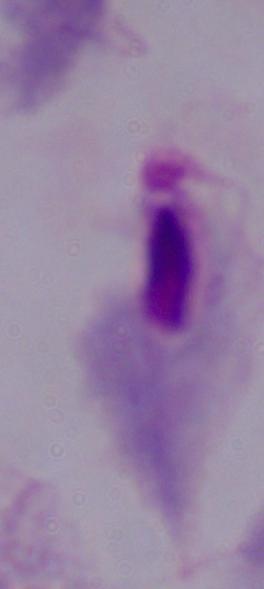

{
  "modality": "micrograph",
  "identification": "trichomonad",
  "magnification": "1000x"
}